Evaluate for malaria.
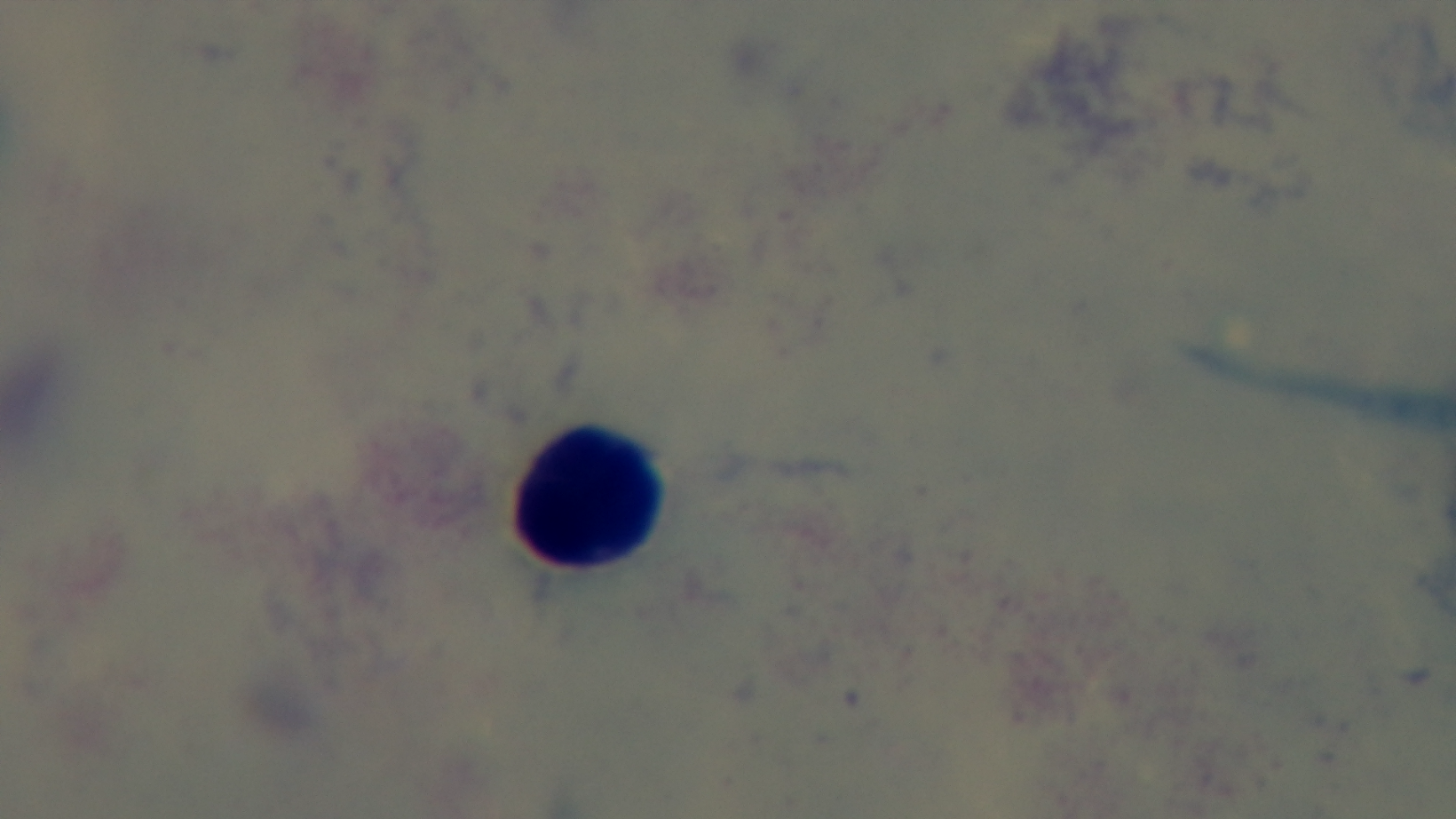

Uninfected.

Summary:
  - Field of view: single
  - Preparation: thick smear
  - Capture: mounted 4K digital camera
  - Modality: light microscopy
  - Stain: Giemsa
  - Objective: 100x oil immersion